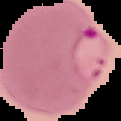

Summary:
  - Preparation: thin blood smear
  - Result: Plasmodium parasites identified
  - Image size: 121×121 pixels
  - Image type: cell region segmented out of the field of view; surrounding area masked to black